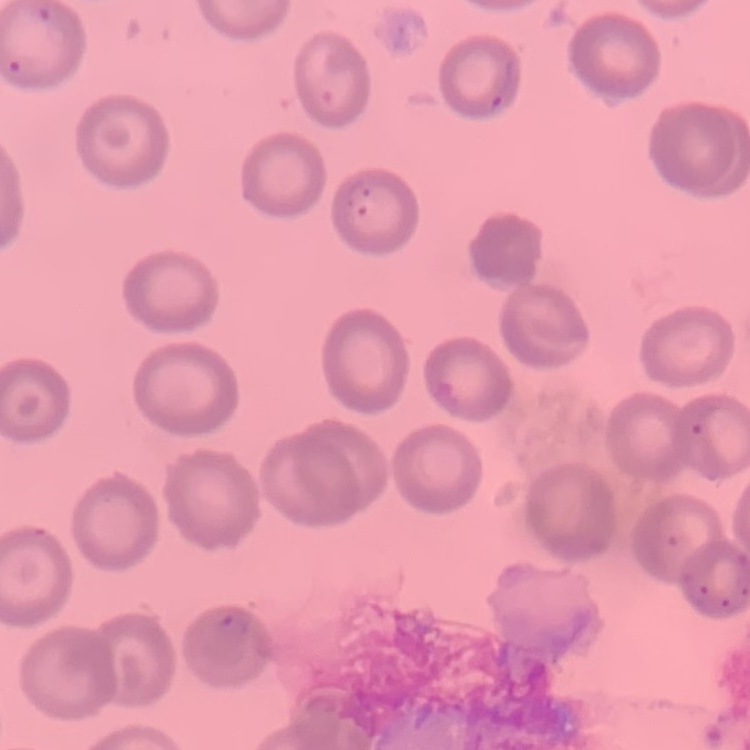
{
  "red_blood_cell_morphology": "no rouleaux formation",
  "image_type": "square crop of a larger photomicrograph",
  "stain": "Field's or Giemsa",
  "preparation": "thin blood film"
}